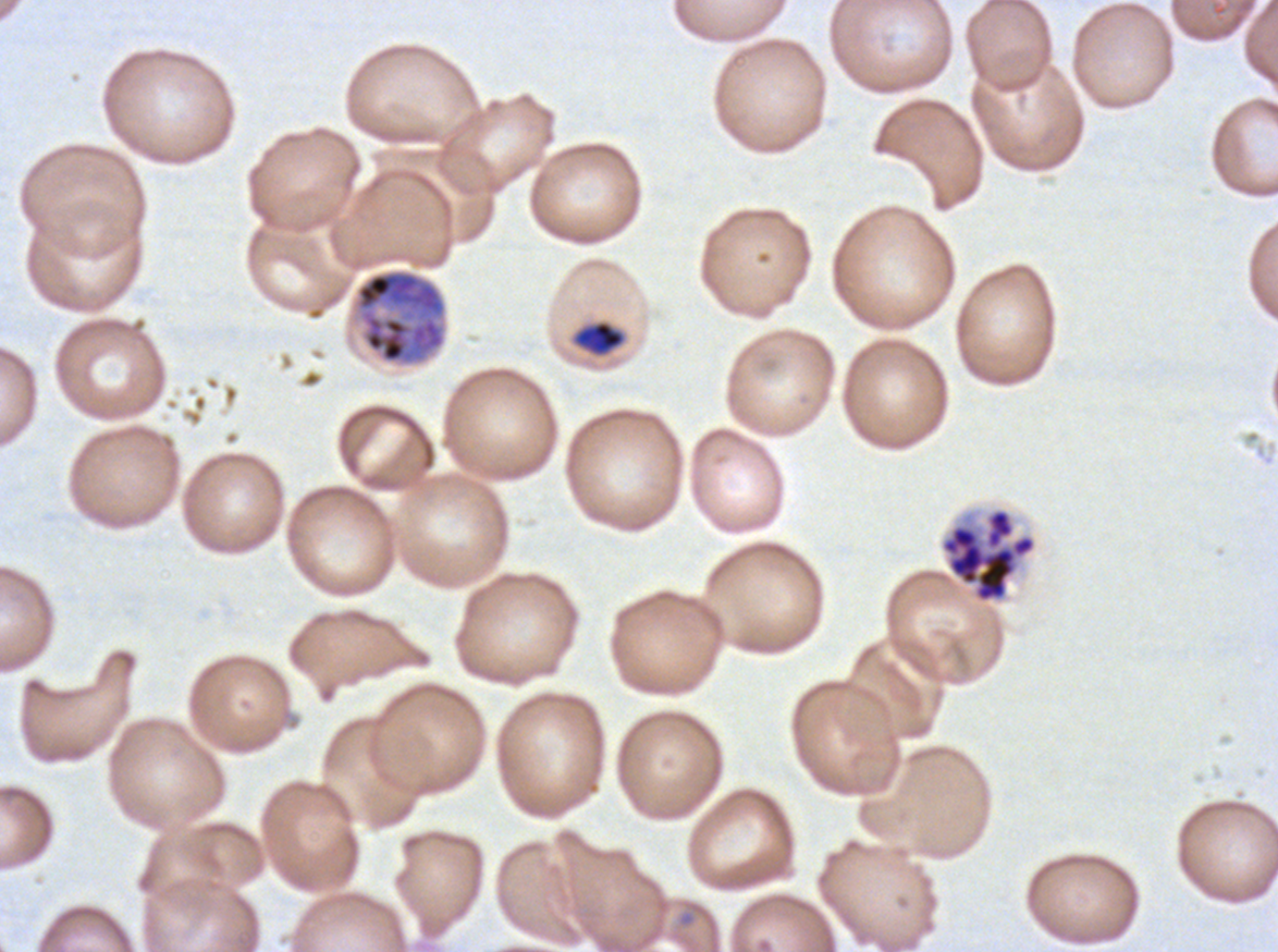
Approximate bounding boxes as {x1, y1, x2, y2} in pixels. Late-ring/early-trophozoite locations: {574, 321, 625, 355}. Segmenter locations: {939, 507, 1038, 604}. Late schizont locations: {355, 269, 446, 364}. Ex-vivo Plasmodium falciparum culture from a patient in The Gambia, grown for 24 to 48 hours. One sub-image of a larger composite. Giemsa stain. Life-cycle stages observed: late-ring/early-trophozoite, late schizont, segmenter. Image is 1278×952 pixels. Thin blood smear.